Classify this cell by malaria status.
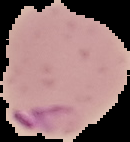
It is parasitized.

Segmented cell region on a black background. Image is 130×142 pixels. From a thin blood smear.